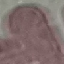 Result: negative for malaria parasites. Giemsa-stained preparation. Cell patch, automatically extracted from a larger field of view and resized to 64 × 64 pixels. Acquired by smartphone through the microscope eyepiece. Thin smear of blood.